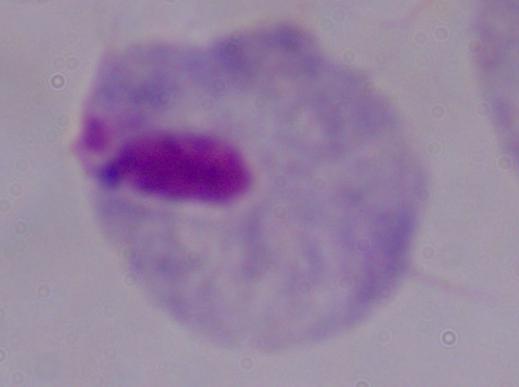
1000x magnification. Photomicrograph. A trichomonad is seen.